Report the malaria status of this cell.
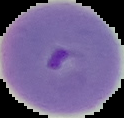

It is parasitized.

Summary:
  - Image type: segmented cell region on a black background
  - Image size: 124×118 pixels
  - Preparation: thin blood film